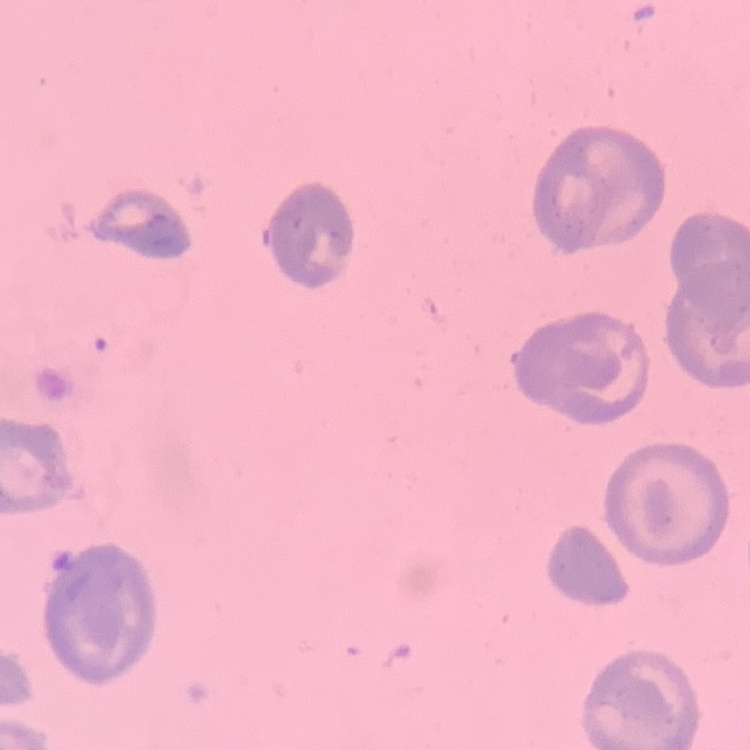
{
  "red_blood_cell_morphology": "no rouleaux formation",
  "image_type": "one tile cut from a larger photomicrograph",
  "preparation": "thin blood film",
  "stain": "Field's or Giemsa"
}